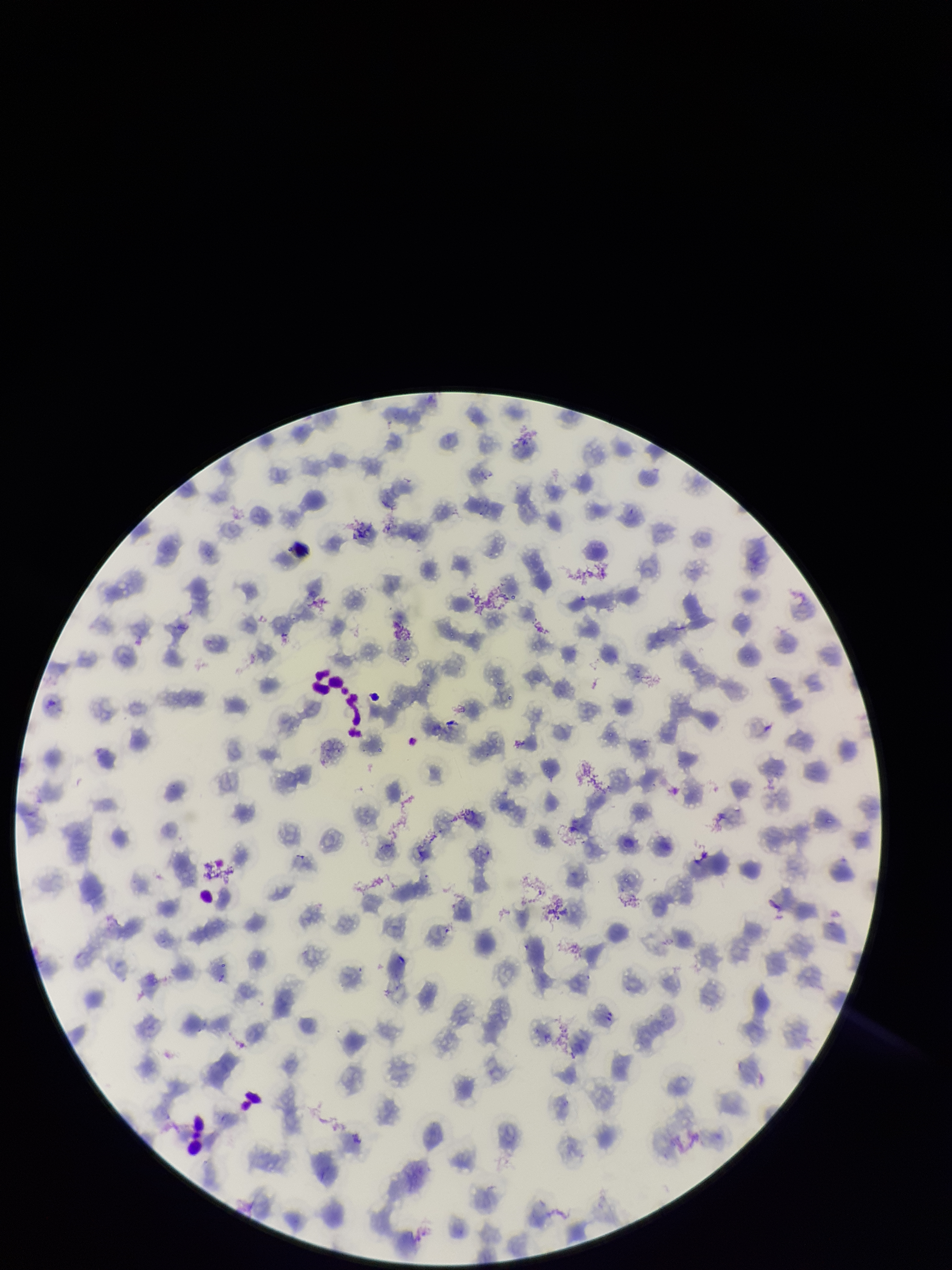 Image is 952×1270 pixels. Smartphone photograph taken through the eyepiece of a microscope. Parasitized red blood cells: none seen. Giemsa stain. Species reported for this patient: Plasmodium falciparum. Red blood cell count: 155. One field from this slide. Preparation: thin smear. Parasitized red blood cell count: 0. Patient malaria status: infected.